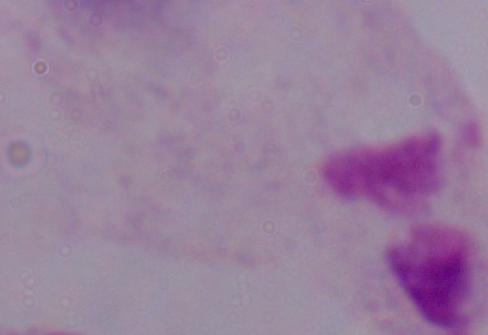

magnification = 1000x
modality = micrograph
identification = trichomonad